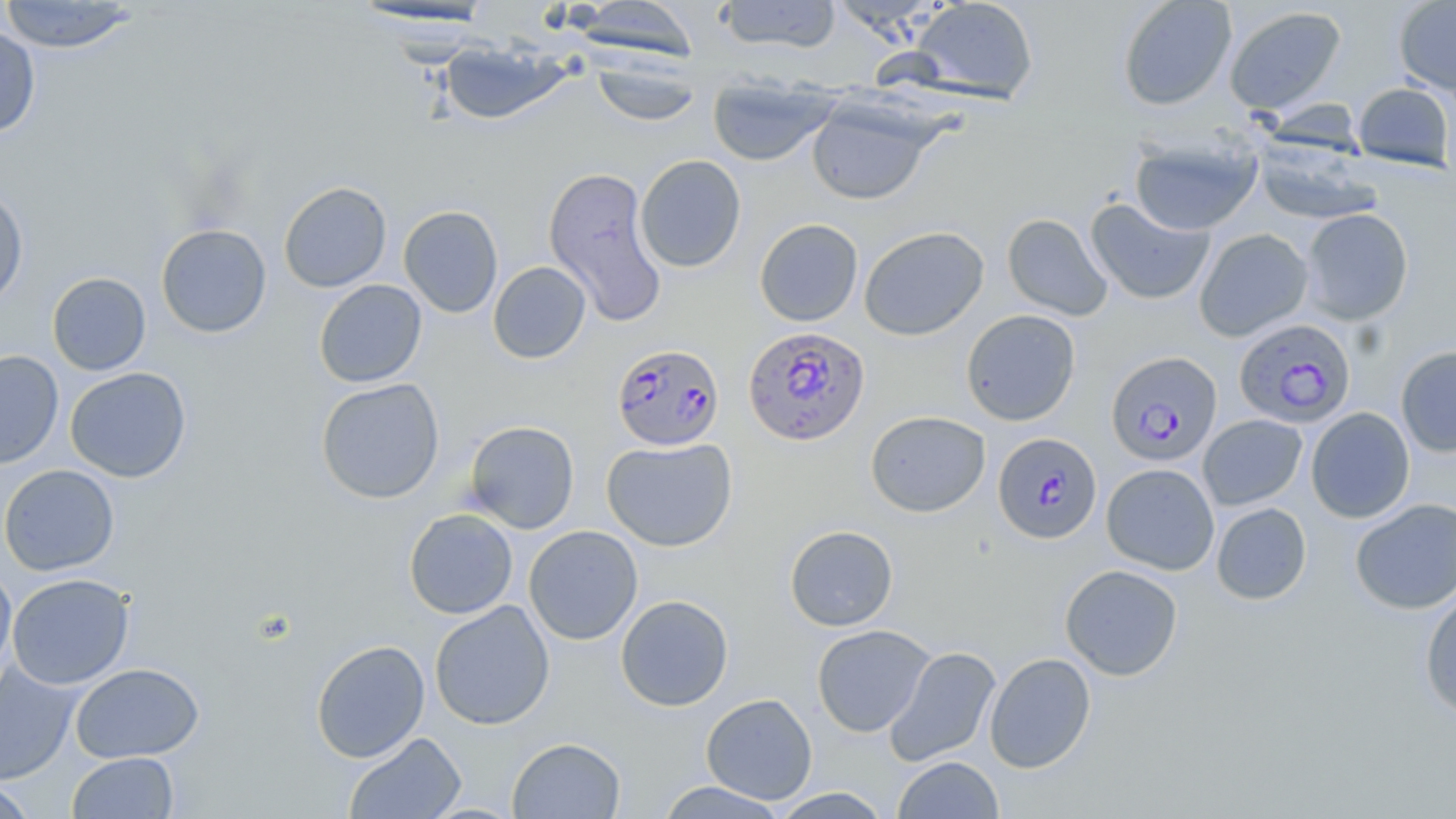

slide-level diagnosis = Plasmodium falciparum
magnification = 1000x
Plasmodium falciparum-infected red blood cell locations = approximate bounding boxes as (x1, y1, x2, y2) in pixels: (1235, 319, 1357, 428), (743, 325, 871, 446), (612, 343, 725, 452), (1106, 350, 1223, 466), (993, 432, 1102, 545)
field of view = one of a larger specimen
stain = May-Grünwald-Giemsa
preparation = thin blood smear
image size = 1456×819 pixels
uninfected red blood cell locations = approximate bounding boxes as (x1, y1, x2, y2) in pixels: (0, 0, 138, 53), (715, 0, 842, 53), (909, 0, 1039, 104), (1117, 0, 1237, 111), (1393, 0, 1456, 96), (347, 1, 500, 32), (568, 1, 700, 62), (1223, 5, 1348, 116), (0, 25, 41, 137), (439, 40, 568, 126), (591, 56, 703, 126), (708, 75, 838, 166), (1352, 82, 1454, 171), (806, 98, 935, 205), (1130, 136, 1262, 236), (1253, 139, 1382, 225), (634, 155, 746, 273), (542, 166, 667, 327), (278, 181, 392, 293), (0, 187, 29, 309), (1085, 197, 1215, 305), (399, 205, 503, 318), (1300, 208, 1414, 325), (1002, 213, 1113, 321), (754, 219, 863, 326), (156, 224, 272, 338), (858, 226, 989, 341), (1194, 228, 1314, 342), (488, 261, 591, 363), (47, 272, 151, 375), (314, 279, 427, 388), (961, 309, 1080, 425), (1395, 345, 1456, 457), (0, 350, 64, 470), (65, 367, 191, 483), (316, 377, 445, 504), (1306, 407, 1415, 523), (865, 410, 990, 517), (1198, 415, 1307, 510), (465, 420, 579, 534), (601, 438, 738, 551), (1101, 463, 1219, 575), (0, 464, 120, 576), (1350, 498, 1456, 615), (1211, 502, 1312, 605), (403, 508, 518, 619), (523, 525, 643, 645), (784, 525, 898, 632), (1060, 564, 1183, 681), (0, 565, 17, 687), (7, 573, 134, 689), (1420, 589, 1456, 720), (615, 594, 734, 711), (429, 600, 555, 730), (812, 624, 935, 737), (310, 639, 430, 763), (884, 646, 1001, 767), (984, 652, 1096, 773), (0, 661, 81, 786), (70, 662, 204, 763), (702, 693, 818, 804), (344, 732, 466, 819), (507, 737, 626, 818), (67, 752, 179, 818), (892, 756, 1004, 818), (0, 779, 38, 818), (654, 781, 789, 818), (770, 787, 892, 818)
modality = light microscopy